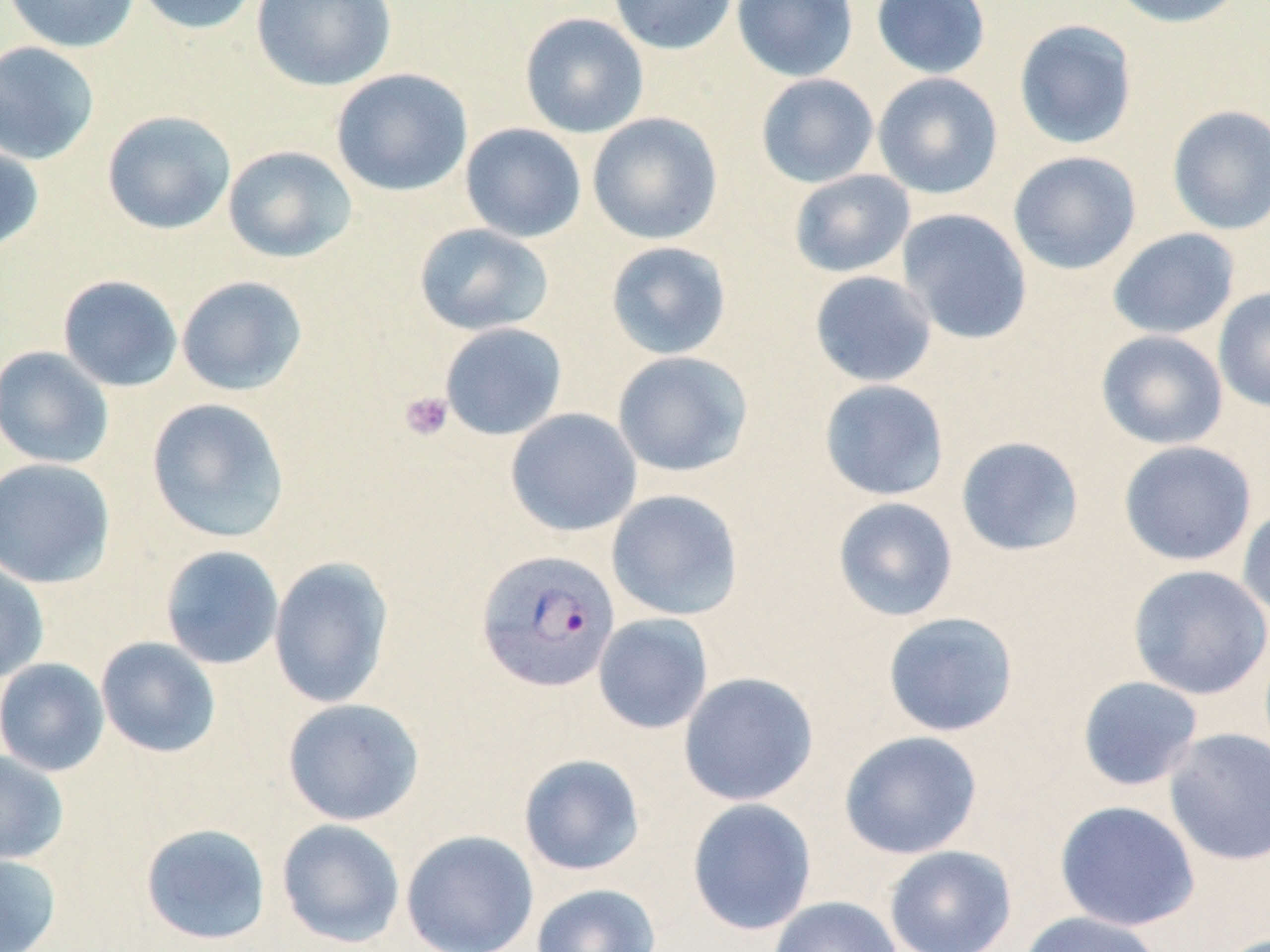 Approximate bounding boxes as (x1, y1, x2, y2) in pixels. Uninfected red blood cell locations: (3, 0, 141, 53), (130, 0, 261, 35), (250, 0, 396, 91), (608, 0, 738, 55), (732, 0, 859, 82), (871, 0, 991, 79), (1105, 0, 1247, 28), (519, 12, 649, 138), (1013, 19, 1138, 150), (0, 41, 101, 165), (331, 68, 473, 197), (872, 72, 1003, 200), (755, 73, 879, 188), (1166, 105, 1270, 235), (101, 110, 236, 235), (587, 112, 723, 245), (460, 123, 586, 243), (0, 141, 44, 254), (222, 145, 357, 263), (1008, 151, 1142, 275), (789, 169, 915, 278), (896, 208, 1033, 345), (413, 223, 554, 336), (1107, 228, 1240, 340), (605, 240, 732, 360), (809, 270, 937, 387), (57, 274, 183, 392), (176, 275, 308, 396), (1213, 287, 1270, 413), (439, 322, 567, 440), (1096, 330, 1228, 450), (0, 346, 115, 469), (612, 351, 753, 477), (818, 379, 950, 501), (145, 397, 291, 544), (505, 408, 642, 537), (955, 436, 1085, 557), (1119, 440, 1257, 566), (0, 457, 116, 589), (606, 489, 744, 621), (832, 496, 959, 622), (1237, 504, 1270, 621), (160, 545, 284, 670), (268, 556, 394, 709), (0, 558, 50, 684), (1127, 564, 1270, 700), (882, 611, 1019, 737), (593, 613, 713, 734), (96, 636, 221, 758), (0, 658, 110, 776), (677, 671, 819, 807), (1077, 675, 1204, 792), (281, 697, 425, 826), (1163, 727, 1270, 865), (839, 730, 983, 859), (0, 749, 69, 865), (518, 753, 646, 876), (686, 798, 817, 936), (1054, 800, 1201, 931), (276, 818, 406, 948), (140, 822, 272, 945), (401, 829, 539, 952), (883, 845, 1017, 952), (0, 853, 62, 952), (531, 884, 662, 952), (768, 895, 902, 952), (1014, 910, 1164, 952). Platelet locations: (399, 391, 453, 441). Plasmodium vivax-infected red blood cell locations: (476, 549, 621, 693). Slide-level diagnosis: Plasmodium vivax. Light microscopy. Thin blood film. May-Grünwald-Giemsa-stained preparation. Image is 1270×952 pixels. Captured at 1000x magnification. One field of a larger specimen.